Identify the parasite.
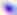

Toxoplasma gondii.

Summary:
  - Magnification: 400x
  - Modality: photomicrograph